Report the malaria status of this cell.
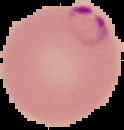

It is parasitized.

Summary:
  - Image type: segmented cell region with the area outside set to black
  - Preparation: thin blood smear
  - Image size: 124×130 pixels